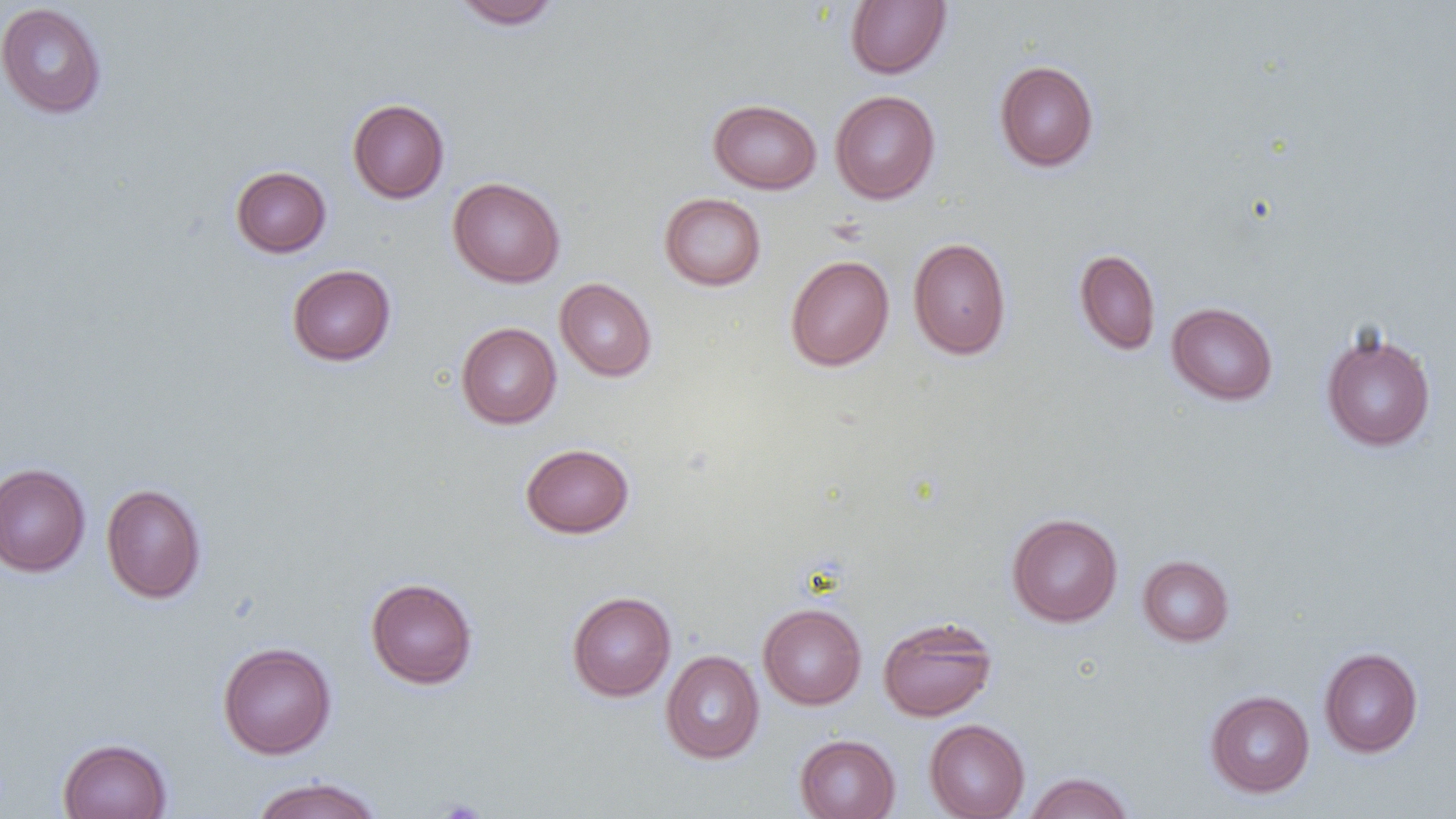

Approximate bounding boxes as (x1,y1)-(x2,y2) corner pairs in pixels. Uninfected red blood cell locations: (452,0)-(563,30), (845,0)-(951,79), (0,2)-(107,119), (994,60)-(1099,172), (829,89)-(940,204), (347,98)-(449,203), (708,99)-(821,194), (230,166)-(331,257), (447,176)-(565,288), (659,193)-(767,291), (907,237)-(1012,359), (1074,249)-(1160,355), (785,254)-(894,371), (287,264)-(396,365), (555,278)-(657,382), (1167,302)-(1278,405), (455,322)-(562,428), (1320,329)-(1437,452), (520,443)-(635,538), (0,462)-(90,577), (101,483)-(207,604), (1006,513)-(1123,627), (1137,554)-(1234,646), (365,577)-(478,689), (566,591)-(676,701), (758,602)-(867,709), (877,616)-(997,722), (217,641)-(336,759), (1319,647)-(1423,757), (661,650)-(764,763), (1205,690)-(1315,797), (924,719)-(1030,819), (794,734)-(901,819), (57,737)-(172,819), (1023,771)-(1134,819), (249,776)-(384,819). Slide-level diagnosis: no evidence of blood parasites. Optical microscopy. Image is 1456×819 pixels. Captured at 1000x magnification. Single field of view. Thin blood smear.